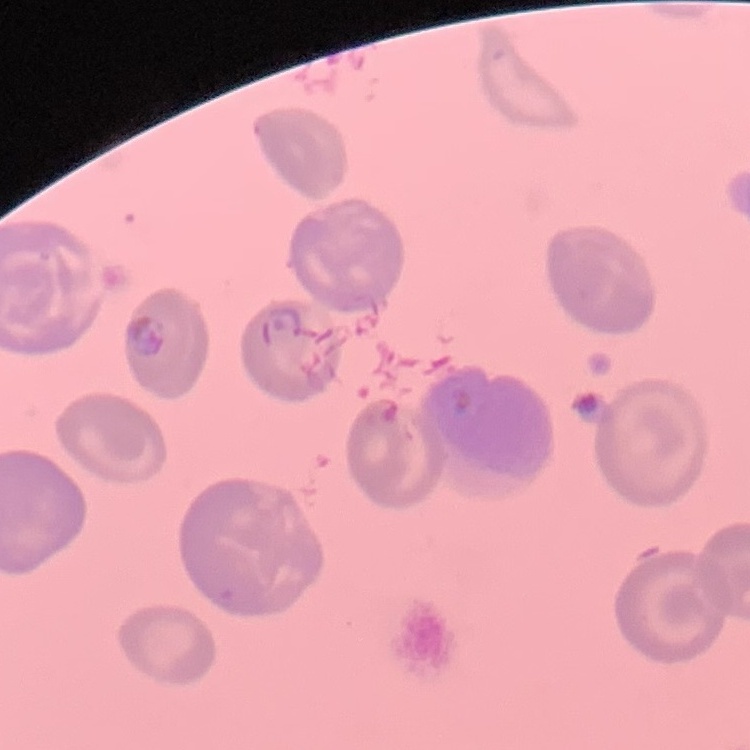

Summary:
  - Red blood cell morphology: no rouleaux formation
  - Preparation: thin peripheral smear
  - Stain: Field's or Giemsa
  - Image type: one tile cut from a larger photomicrograph